Give the extent of all white blood cells.
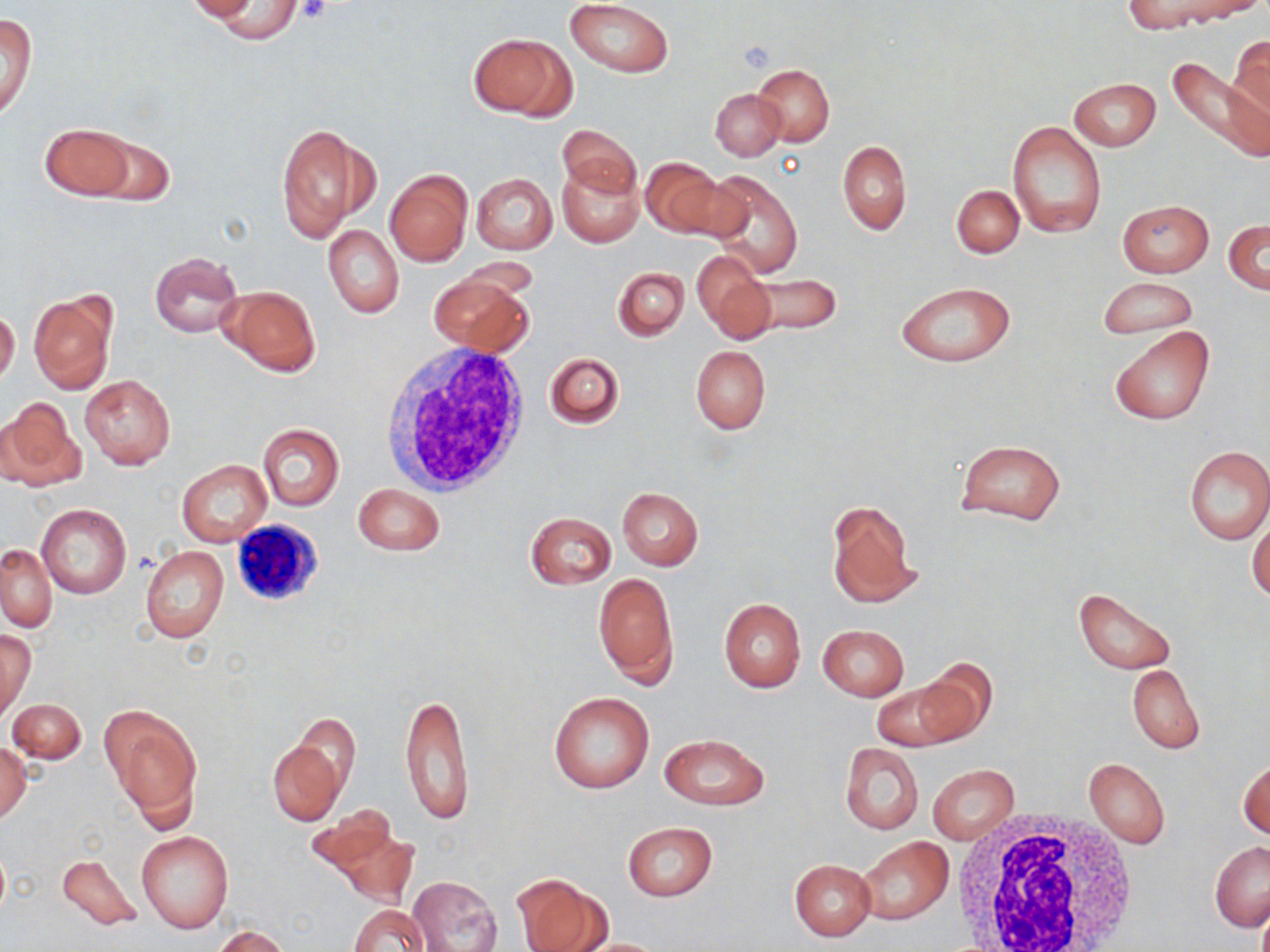
Approximate bounding boxes as named x1/y1/x2/y2 corners in pixels.
White blood cells: (x1=381, y1=342, x2=532, y2=499), (x1=232, y1=512, x2=334, y2=611), (x1=949, y1=811, x2=1139, y2=952).

Summary:
  - Platelet locations: (x1=297, y1=0, x2=330, y2=23), (x1=737, y1=41, x2=775, y2=74)
  - Uninfected red blood cell locations: (x1=566, y1=0, x2=674, y2=77), (x1=1121, y1=0, x2=1230, y2=31), (x1=1188, y1=0, x2=1267, y2=17), (x1=181, y1=1, x2=260, y2=22), (x1=210, y1=2, x2=304, y2=42), (x1=1, y1=14, x2=36, y2=123), (x1=472, y1=33, x2=572, y2=121), (x1=1230, y1=33, x2=1270, y2=128), (x1=1169, y1=58, x2=1268, y2=169), (x1=752, y1=64, x2=834, y2=147), (x1=1069, y1=78, x2=1159, y2=151), (x1=711, y1=88, x2=787, y2=160), (x1=1006, y1=121, x2=1105, y2=238), (x1=38, y1=123, x2=135, y2=199), (x1=276, y1=123, x2=372, y2=243), (x1=557, y1=123, x2=640, y2=200), (x1=84, y1=134, x2=175, y2=206), (x1=837, y1=140, x2=911, y2=235), (x1=641, y1=156, x2=726, y2=238), (x1=558, y1=162, x2=643, y2=248), (x1=385, y1=169, x2=472, y2=267), (x1=701, y1=169, x2=804, y2=278), (x1=470, y1=172, x2=558, y2=254), (x1=951, y1=185, x2=1024, y2=258), (x1=1117, y1=200, x2=1214, y2=276), (x1=1224, y1=220, x2=1270, y2=292), (x1=323, y1=225, x2=404, y2=318), (x1=694, y1=251, x2=773, y2=343), (x1=150, y1=252, x2=242, y2=338), (x1=612, y1=266, x2=689, y2=341), (x1=736, y1=271, x2=842, y2=337), (x1=429, y1=274, x2=534, y2=357), (x1=1097, y1=277, x2=1198, y2=338), (x1=895, y1=281, x2=1017, y2=367), (x1=219, y1=285, x2=320, y2=374), (x1=27, y1=291, x2=117, y2=396), (x1=0, y1=308, x2=20, y2=386), (x1=1111, y1=326, x2=1215, y2=427), (x1=690, y1=345, x2=771, y2=434), (x1=544, y1=351, x2=624, y2=428), (x1=79, y1=375, x2=176, y2=470), (x1=0, y1=398, x2=85, y2=490), (x1=256, y1=423, x2=345, y2=511), (x1=954, y1=439, x2=1067, y2=525), (x1=1183, y1=445, x2=1270, y2=543), (x1=178, y1=459, x2=270, y2=548), (x1=353, y1=484, x2=445, y2=556), (x1=616, y1=487, x2=704, y2=570), (x1=826, y1=500, x2=919, y2=608), (x1=36, y1=503, x2=131, y2=599), (x1=526, y1=512, x2=617, y2=590), (x1=1248, y1=514, x2=1270, y2=604), (x1=1, y1=544, x2=55, y2=632), (x1=140, y1=545, x2=229, y2=643), (x1=594, y1=572, x2=678, y2=688), (x1=1075, y1=587, x2=1176, y2=675), (x1=719, y1=598, x2=806, y2=692), (x1=817, y1=624, x2=909, y2=700), (x1=1, y1=631, x2=34, y2=719), (x1=910, y1=661, x2=997, y2=744), (x1=1127, y1=665, x2=1206, y2=754), (x1=871, y1=681, x2=963, y2=752), (x1=399, y1=689, x2=475, y2=825), (x1=548, y1=691, x2=655, y2=794), (x1=8, y1=698, x2=86, y2=764), (x1=105, y1=708, x2=201, y2=824), (x1=290, y1=713, x2=361, y2=797), (x1=660, y1=734, x2=768, y2=811), (x1=267, y1=735, x2=346, y2=825), (x1=0, y1=740, x2=32, y2=824), (x1=838, y1=742, x2=924, y2=835), (x1=1083, y1=758, x2=1170, y2=849), (x1=1238, y1=758, x2=1270, y2=840), (x1=927, y1=765, x2=1019, y2=842), (x1=306, y1=806, x2=411, y2=895), (x1=622, y1=821, x2=718, y2=901), (x1=136, y1=831, x2=234, y2=935), (x1=856, y1=837, x2=954, y2=927), (x1=1210, y1=841, x2=1269, y2=931), (x1=57, y1=853, x2=142, y2=931), (x1=789, y1=858, x2=876, y2=941), (x1=512, y1=872, x2=612, y2=952), (x1=408, y1=876, x2=503, y2=952), (x1=348, y1=903, x2=428, y2=952), (x1=213, y1=925, x2=292, y2=951), (x1=565, y1=937, x2=674, y2=952)
  - Slide-level diagnosis: negative for blood parasites
  - Preparation: thin blood film
  - Stain: May-Grünwald-Giemsa
  - Modality: light microscopy
  - Field of view: single
  - Magnification: 1000x
  - Image size: 1270×952 pixels